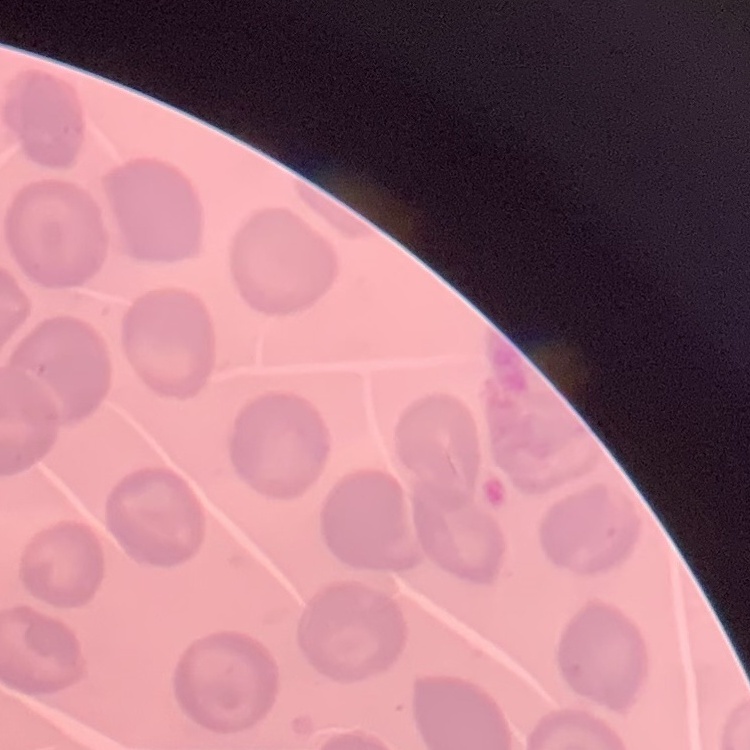
red blood cell morphology = no rouleaux formation
preparation = thin blood film
image type = one tile cut from a larger photomicrograph
stain = Field's or Giemsa